Describe the morphology of the erythrocytes.
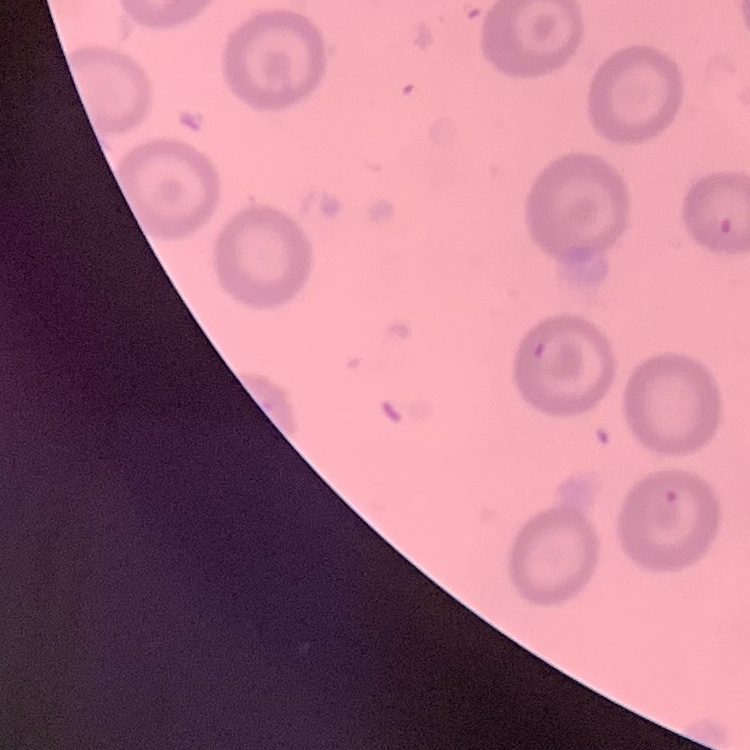
They show no rouleaux formation.

Square crop of a larger photomicrograph. Thin blood film. Stained with either Field's or Giemsa.